Assess the morphology of the erythrocytes.
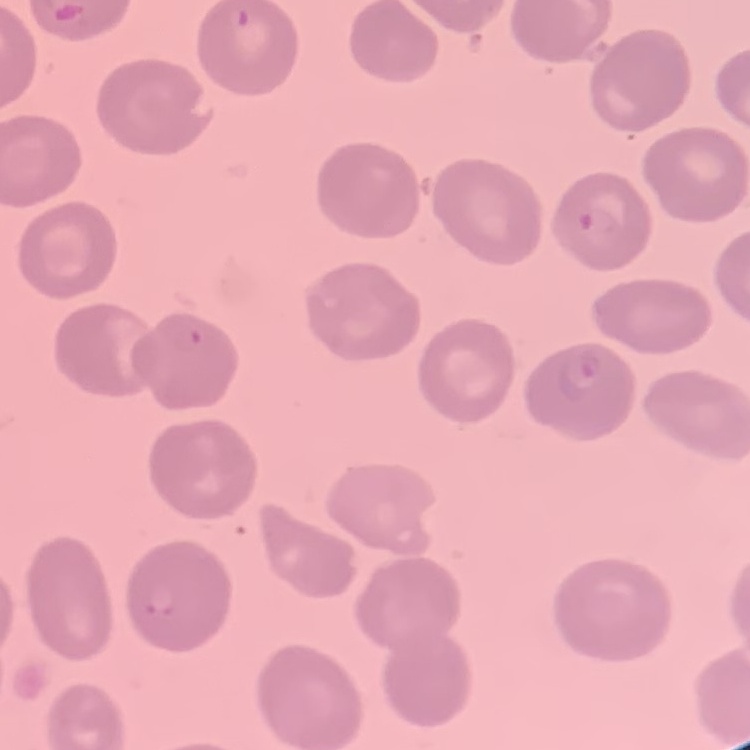

They show no rouleaux formation.

image type = one tile cut from a larger photomicrograph
stain = Field's or Giemsa
preparation = thin peripheral smear